Report the malaria status of this cell.
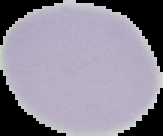
Uninfected.

Segmented cell region on a black background. Image is 163×136 pixels. From a thin blood film.